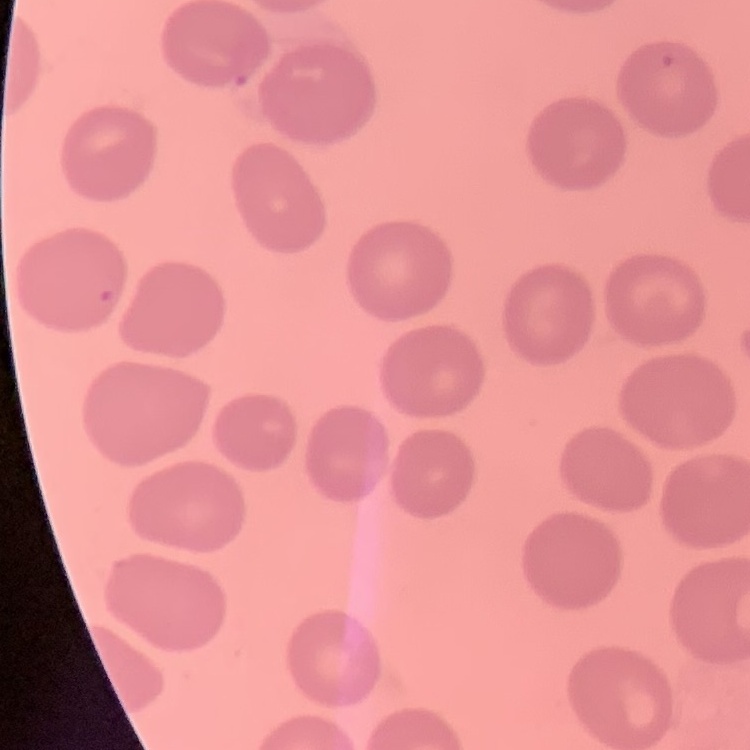

red_blood_cell_morphology: no rouleaux formation
stain: Field's or Giemsa
preparation: thin blood film
image_type: square crop of a larger photomicrograph